Classify this cell by malaria status.
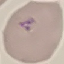

Parasitized.

Thin smear of blood. Photographed with a smartphone camera at the microscope eyepiece. Cell patch, automatically extracted from a larger field of view and resized to 64 × 64 pixels. Giemsa-stained preparation.